Give the extent of all white blood cells.
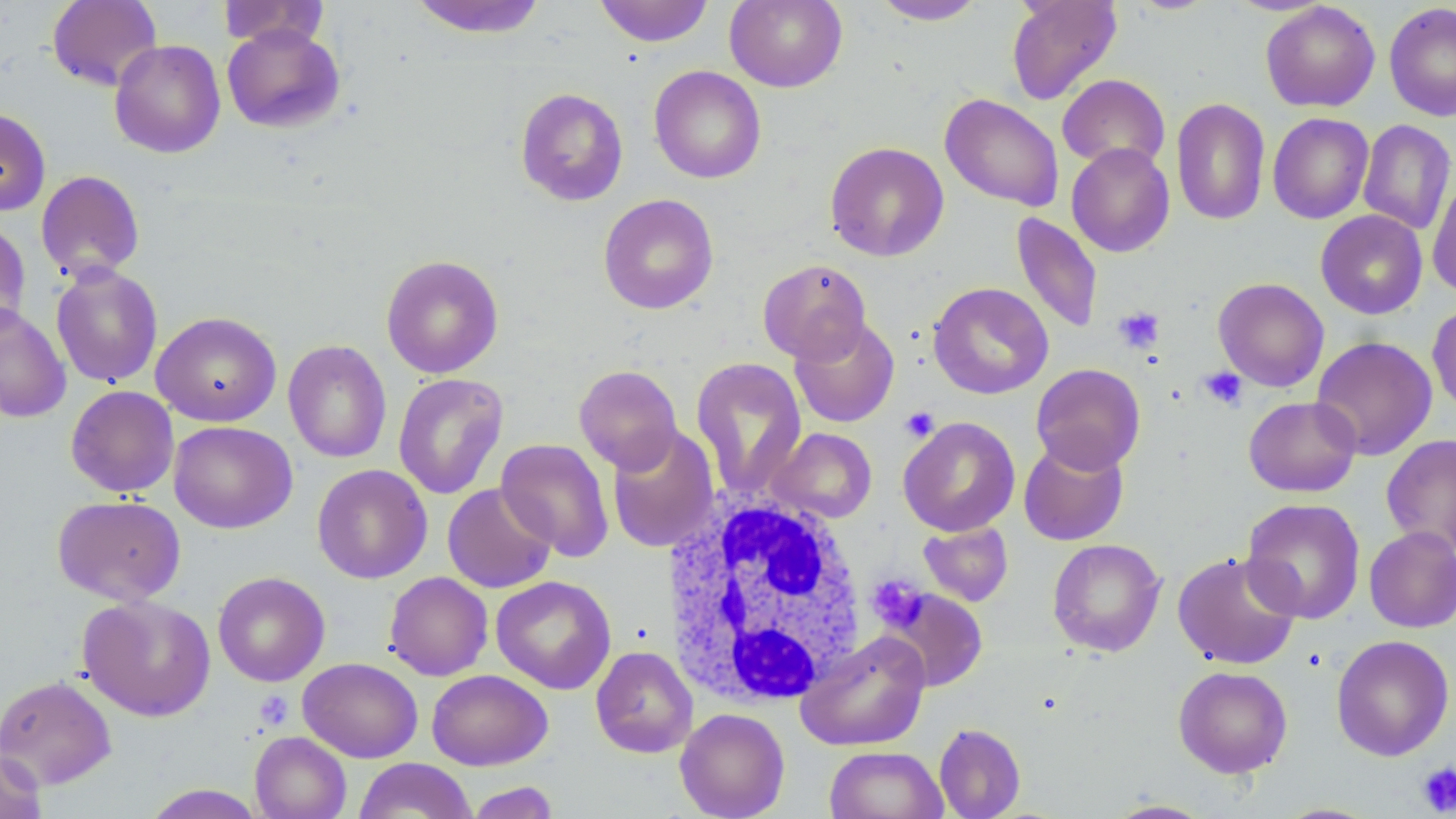
Approximate bounding boxes as named x1/y1/x2/y2 corners in pixels.
White blood cells: (x1=659, y1=490, x2=872, y2=708).

Uninfected red blood cell locations: (x1=47, y1=0, x2=163, y2=91), (x1=408, y1=0, x2=548, y2=39), (x1=594, y1=0, x2=713, y2=47), (x1=725, y1=0, x2=848, y2=92), (x1=871, y1=0, x2=987, y2=25), (x1=1005, y1=0, x2=1122, y2=106), (x1=1126, y1=0, x2=1221, y2=15), (x1=218, y1=1, x2=329, y2=50), (x1=1260, y1=2, x2=1380, y2=112), (x1=1384, y1=2, x2=1456, y2=122), (x1=222, y1=24, x2=345, y2=133), (x1=110, y1=39, x2=226, y2=158), (x1=649, y1=65, x2=766, y2=184), (x1=1057, y1=74, x2=1170, y2=173), (x1=515, y1=87, x2=629, y2=206), (x1=939, y1=93, x2=1064, y2=212), (x1=1171, y1=98, x2=1271, y2=225), (x1=0, y1=107, x2=51, y2=216), (x1=1268, y1=112, x2=1374, y2=224), (x1=1358, y1=120, x2=1455, y2=235), (x1=824, y1=141, x2=950, y2=262), (x1=1066, y1=143, x2=1175, y2=258), (x1=35, y1=170, x2=145, y2=282), (x1=1427, y1=171, x2=1456, y2=298), (x1=598, y1=194, x2=719, y2=314), (x1=1316, y1=209, x2=1428, y2=319), (x1=1011, y1=212, x2=1104, y2=334), (x1=0, y1=219, x2=32, y2=336), (x1=381, y1=255, x2=504, y2=378), (x1=757, y1=258, x2=871, y2=364), (x1=50, y1=263, x2=163, y2=388), (x1=1213, y1=277, x2=1329, y2=392), (x1=928, y1=282, x2=1053, y2=399), (x1=0, y1=302, x2=71, y2=422), (x1=1427, y1=302, x2=1456, y2=417), (x1=151, y1=311, x2=282, y2=427), (x1=789, y1=317, x2=900, y2=428), (x1=1311, y1=336, x2=1437, y2=460), (x1=282, y1=340, x2=392, y2=463), (x1=691, y1=358, x2=807, y2=500), (x1=1031, y1=363, x2=1146, y2=474), (x1=573, y1=365, x2=683, y2=474), (x1=393, y1=372, x2=509, y2=500), (x1=66, y1=385, x2=179, y2=497), (x1=1243, y1=395, x2=1361, y2=497), (x1=898, y1=416, x2=1020, y2=536), (x1=169, y1=420, x2=297, y2=533), (x1=606, y1=425, x2=720, y2=553), (x1=768, y1=427, x2=877, y2=523), (x1=1381, y1=434, x2=1456, y2=554), (x1=1018, y1=437, x2=1129, y2=546), (x1=496, y1=438, x2=614, y2=561), (x1=312, y1=464, x2=432, y2=584), (x1=442, y1=482, x2=557, y2=593), (x1=52, y1=494, x2=186, y2=605), (x1=1241, y1=498, x2=1366, y2=624), (x1=919, y1=522, x2=1013, y2=606), (x1=1364, y1=526, x2=1456, y2=633), (x1=1048, y1=538, x2=1166, y2=656), (x1=1172, y1=551, x2=1302, y2=670), (x1=213, y1=571, x2=330, y2=687), (x1=384, y1=572, x2=493, y2=680), (x1=490, y1=575, x2=616, y2=695), (x1=883, y1=588, x2=988, y2=691), (x1=77, y1=594, x2=217, y2=722), (x1=795, y1=631, x2=931, y2=751), (x1=1331, y1=634, x2=1455, y2=761), (x1=591, y1=646, x2=698, y2=758), (x1=298, y1=657, x2=423, y2=762), (x1=1173, y1=665, x2=1293, y2=778), (x1=427, y1=669, x2=553, y2=771), (x1=0, y1=674, x2=117, y2=790), (x1=674, y1=707, x2=790, y2=819), (x1=934, y1=723, x2=1026, y2=819), (x1=250, y1=731, x2=351, y2=819), (x1=825, y1=746, x2=948, y2=819), (x1=0, y1=747, x2=47, y2=819), (x1=354, y1=758, x2=477, y2=819), (x1=465, y1=781, x2=561, y2=818), (x1=141, y1=784, x2=266, y2=819), (x1=1104, y1=799, x2=1215, y2=818). Platelet locations: (x1=1113, y1=306, x2=1165, y2=354), (x1=1199, y1=366, x2=1249, y2=411), (x1=899, y1=406, x2=939, y2=442), (x1=865, y1=574, x2=928, y2=633), (x1=255, y1=691, x2=294, y2=730), (x1=1416, y1=762, x2=1456, y2=816). Slide-level diagnosis: negative for blood parasites. Captured at 1000x magnification. Image is 1456×819 pixels. Single field of view. Thin blood film. May-Grünwald-Giemsa-stained preparation. Optical microscopy.